Locate and identify every blood parasite.
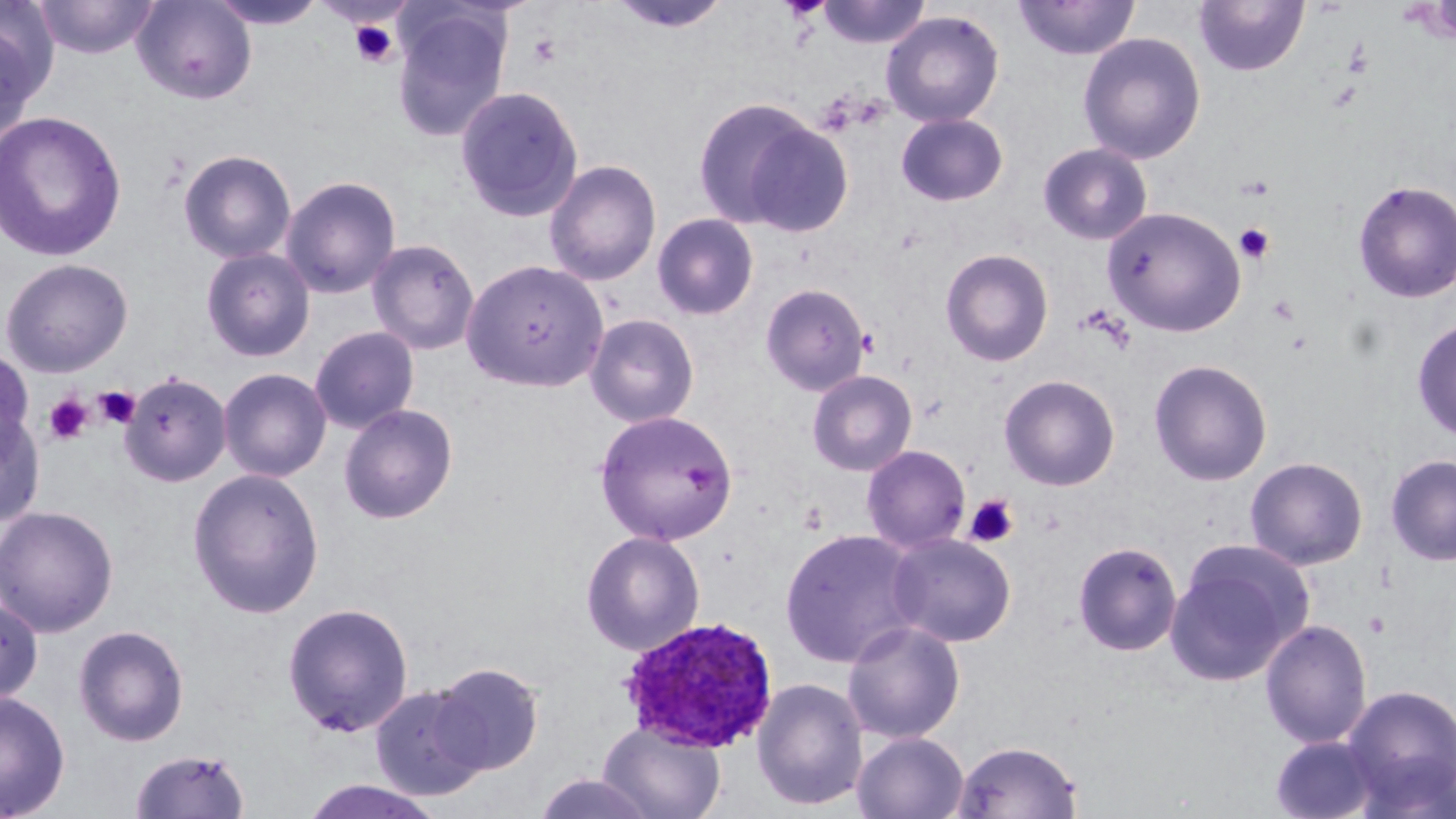
Approximate bounding boxes as (x1, y1, x2, y2) in pixels.
Plasmodium ovale-infected red blood cells: (619, 616, 777, 753).
No Plasmodium falciparum, Plasmodium malariae, Plasmodium vivax, Babesia divergens, or Trypanosoma brucei observed.

Platelet locations: (348, 19, 400, 69), (1240, 175, 1275, 200), (1234, 223, 1275, 264), (1267, 294, 1300, 326), (94, 385, 141, 429), (45, 394, 93, 444), (965, 494, 1019, 548), (1364, 611, 1390, 637). Uninfected red blood cell locations: (32, 0, 160, 59), (132, 0, 257, 105), (209, 0, 329, 30), (816, 0, 932, 49), (1013, 0, 1140, 61), (607, 1, 733, 35), (1192, 1, 1310, 77), (0, 3, 54, 139), (390, 4, 512, 143), (880, 10, 1004, 128), (1077, 32, 1206, 165), (455, 85, 584, 222), (691, 97, 843, 235), (0, 109, 127, 263), (895, 113, 1008, 206), (1038, 143, 1153, 245), (178, 149, 296, 264), (544, 159, 661, 287), (280, 175, 401, 299), (1353, 180, 1456, 303), (1101, 206, 1247, 337), (652, 213, 759, 321), (367, 238, 480, 355), (201, 247, 315, 362), (209, 247, 321, 482), (940, 248, 1053, 367), (0, 257, 133, 378), (462, 258, 609, 391), (760, 283, 871, 396), (585, 314, 699, 428), (1412, 318, 1456, 441), (309, 326, 419, 434), (0, 346, 34, 459), (1149, 359, 1273, 486), (218, 368, 332, 482), (806, 369, 917, 476), (121, 372, 231, 486), (999, 374, 1120, 491), (339, 404, 458, 524), (0, 408, 46, 527), (595, 409, 738, 546), (862, 445, 971, 553), (1384, 454, 1456, 566), (1244, 456, 1368, 570), (186, 467, 325, 618), (0, 505, 119, 637), (780, 528, 924, 669), (581, 530, 705, 656), (888, 533, 1016, 647), (1165, 540, 1312, 686), (1072, 541, 1182, 656), (0, 597, 43, 705), (282, 602, 413, 737), (1260, 618, 1372, 749), (842, 620, 965, 744), (73, 624, 190, 747), (430, 663, 545, 776), (752, 677, 868, 811), (369, 683, 490, 801), (1340, 683, 1456, 815), (0, 691, 70, 818), (598, 721, 726, 819), (852, 731, 969, 819), (1270, 734, 1382, 819), (952, 739, 1084, 819), (129, 747, 251, 818), (532, 772, 657, 819), (299, 779, 445, 819). Slide-level diagnosis: Plasmodium ovale. Optical microscopy. Image is 1456×819 pixels. Thin blood film. May-Grünwald-Giemsa-stained preparation. Captured at 1000x magnification. Single field of view.